Assess the morphology of the red blood cells.
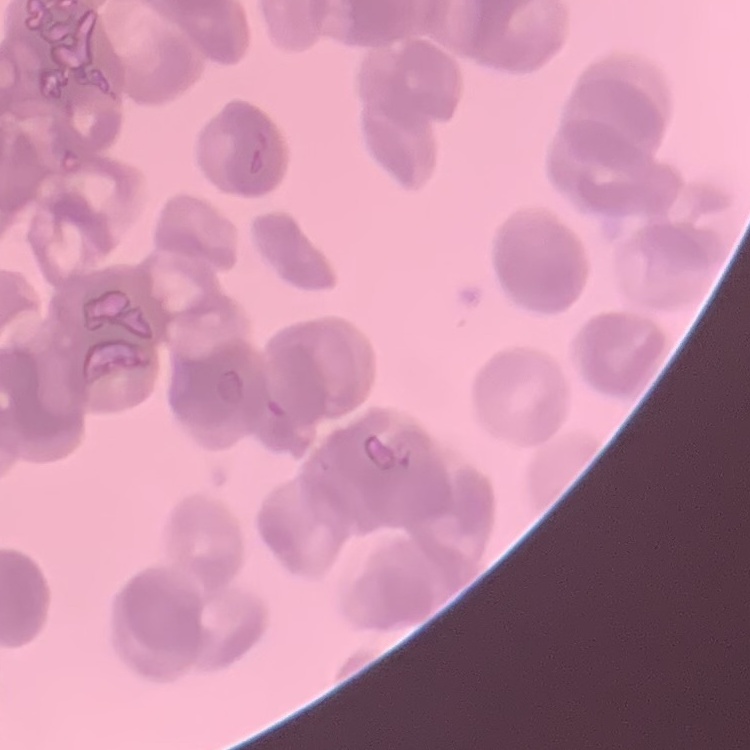

Rouleaux formation.

image type = square crop of a larger photomicrograph
preparation = thin peripheral smear
stain = Field's or Giemsa